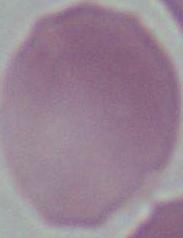 An erythrocyte is shown. Micrograph. Captured at 1000x magnification.